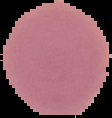 From a thin blood smear. Segmented cell region on a black background. Result: no Plasmodium parasites detected. Image is 112×118 pixels.